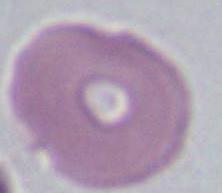

An erythrocyte is shown. Micrograph. Captured at 1000x magnification.